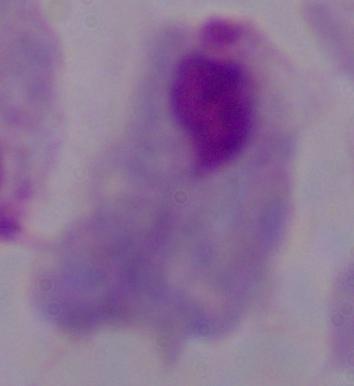

Photomicrograph. Captured at 1000x magnification. A trichomonad is seen.